Assess this cell for malaria.
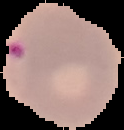

It is parasitized.

From a thin blood film. Segmented cell region on a black background. Image is 124×130 pixels.